Name the parasite shown.
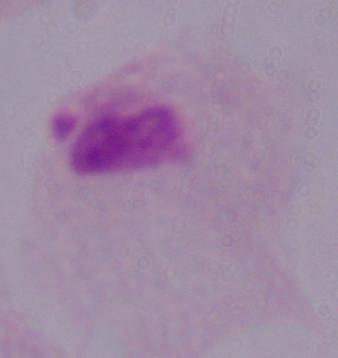

This is a trichomonad.

Summary:
  - Magnification: 1000x
  - Modality: photomicrograph